Identify the parasite.
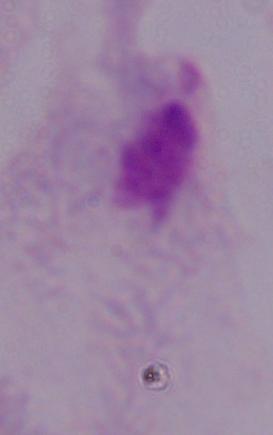

A trichomonad.

Summary:
  - Magnification: 1000x
  - Modality: photomicrograph